Locate and identify every blood parasite.
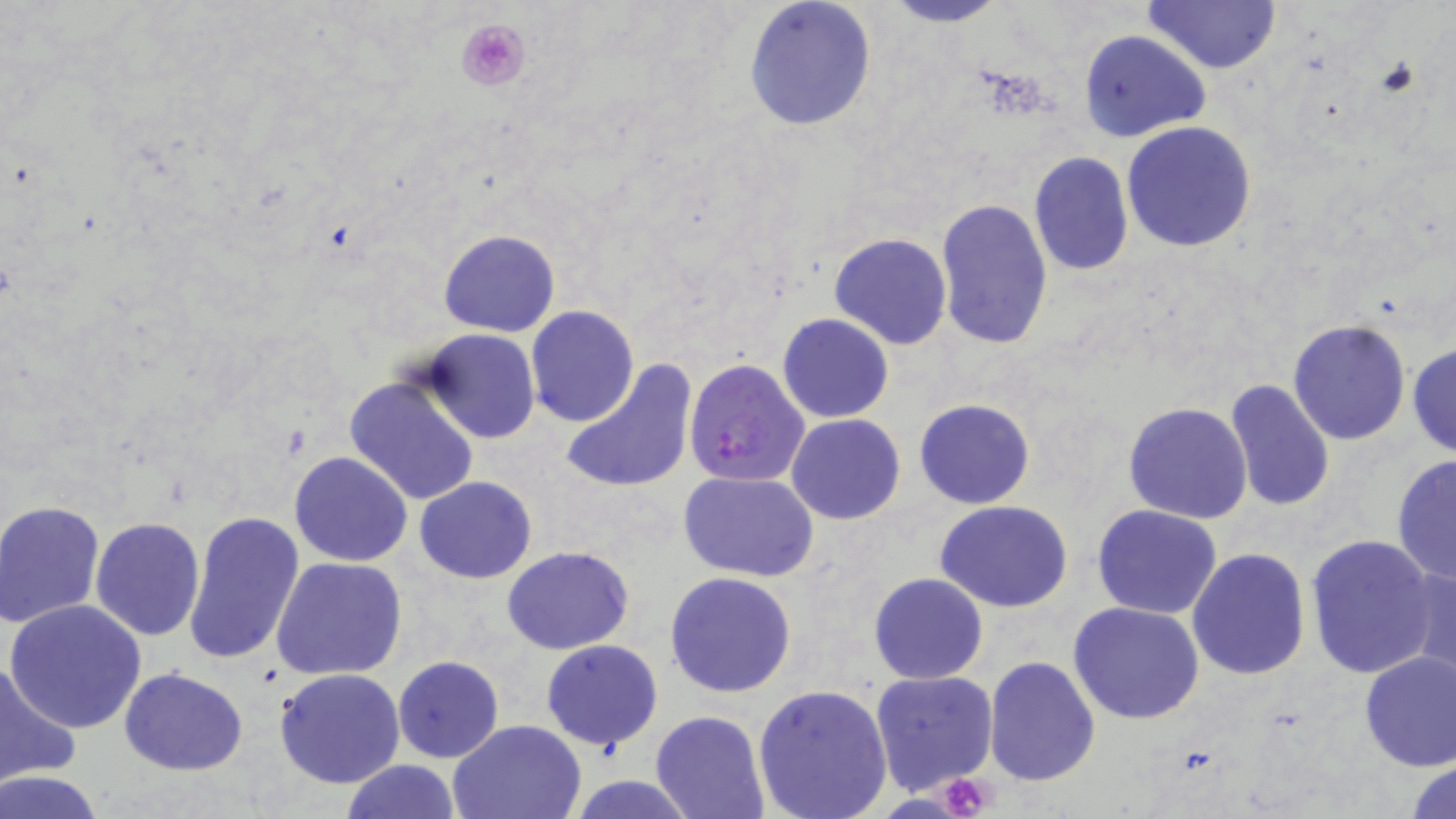
Approximate bounding boxes as (x1, y1, x2, y2) in pixels.
Plasmodium falciparum-infected red blood cells: (684, 357, 811, 487).
No Plasmodium ovale, Plasmodium malariae, Plasmodium vivax, Babesia divergens, or Trypanosoma brucei observed.

{
  "slide_level_diagnosis": "Plasmodium falciparum",
  "preparation": "thin blood film",
  "platelet_locations": "approximate bounding boxes as (x1, y1, x2, y2) in pixels: (454, 16, 532, 93), (932, 774, 997, 818)",
  "modality": "optical microscopy",
  "magnification": "1000x",
  "stain": "May-Grünwald-Giemsa",
  "image_size": "1456×819 pixels",
  "field_of_view": "single",
  "uninfected_red_blood_cell_locations": "approximate bounding boxes as (x1, y1, x2, y2) in pixels: (877, 0, 1010, 27), (1144, 0, 1281, 74), (742, 1, 879, 135), (1080, 29, 1210, 143), (1121, 121, 1255, 253), (1027, 152, 1134, 277), (935, 197, 1054, 349), (438, 228, 560, 338), (829, 233, 951, 350), (525, 305, 639, 427), (777, 314, 894, 423), (1287, 318, 1412, 445), (422, 330, 538, 443), (1407, 341, 1456, 457), (559, 358, 698, 495), (343, 375, 481, 506), (1225, 378, 1335, 515), (914, 397, 1035, 509), (1123, 401, 1252, 524), (786, 406, 1036, 513), (787, 414, 906, 524), (289, 450, 414, 566), (1390, 453, 1456, 588), (679, 471, 819, 581), (414, 476, 538, 584), (0, 500, 105, 626), (935, 500, 1073, 612), (1092, 504, 1223, 618), (183, 511, 304, 665), (92, 517, 206, 640), (1305, 534, 1442, 677), (502, 545, 634, 654), (1187, 549, 1311, 681), (271, 556, 408, 681), (1402, 564, 1456, 688), (665, 570, 798, 698), (868, 572, 988, 684), (3, 599, 149, 735), (1068, 601, 1207, 723), (541, 640, 664, 750), (1358, 651, 1456, 771), (392, 655, 504, 763), (985, 657, 1101, 787), (0, 662, 79, 789), (119, 666, 247, 775), (276, 668, 404, 788), (869, 669, 998, 794), (754, 683, 892, 818), (651, 711, 769, 819), (448, 719, 590, 818), (1406, 757, 1456, 818), (339, 760, 462, 819), (1, 772, 106, 818), (567, 776, 699, 817)"
}